Classify this cell by malaria status.
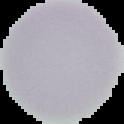

It is uninfected.

Summary:
  - Image size: 124×124 pixels
  - Image type: segmented cell region with the area outside set to black
  - Preparation: thin blood film